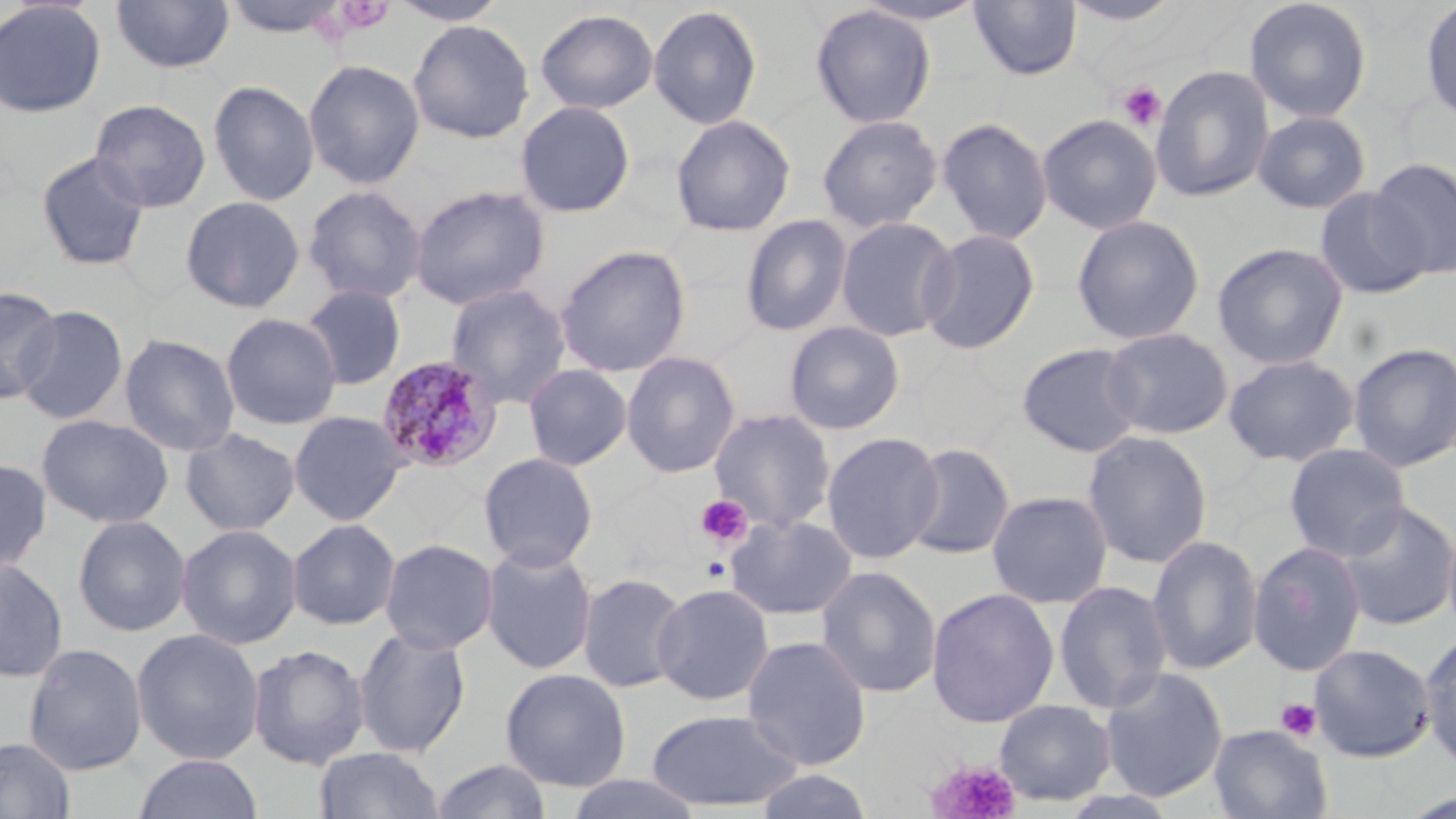

Summary:
  - Coordinate format: approximate bounding boxes as named x1/y1/x2/y2 corners in pixels
  - Uninfected red blood cell locations: (x1=111, y1=0, x2=234, y2=75), (x1=222, y1=0, x2=350, y2=38), (x1=388, y1=0, x2=509, y2=26), (x1=1243, y1=0, x2=1373, y2=123), (x1=0, y1=1, x2=107, y2=118), (x1=968, y1=1, x2=1082, y2=81), (x1=1060, y1=1, x2=1184, y2=28), (x1=1419, y1=1, x2=1456, y2=128), (x1=648, y1=4, x2=762, y2=129), (x1=810, y1=4, x2=936, y2=128), (x1=535, y1=8, x2=658, y2=114), (x1=408, y1=19, x2=534, y2=143), (x1=303, y1=59, x2=425, y2=189), (x1=1151, y1=64, x2=1275, y2=203), (x1=207, y1=79, x2=320, y2=206), (x1=89, y1=99, x2=211, y2=213), (x1=515, y1=101, x2=636, y2=218), (x1=1252, y1=110, x2=1371, y2=214), (x1=816, y1=114, x2=943, y2=232), (x1=1037, y1=114, x2=1163, y2=234), (x1=670, y1=115, x2=796, y2=237), (x1=937, y1=117, x2=1053, y2=245), (x1=36, y1=152, x2=150, y2=272), (x1=1369, y1=157, x2=1456, y2=280), (x1=302, y1=184, x2=428, y2=305), (x1=409, y1=185, x2=550, y2=310), (x1=1314, y1=187, x2=1432, y2=299), (x1=180, y1=195, x2=305, y2=313), (x1=740, y1=214, x2=853, y2=336), (x1=1071, y1=214, x2=1205, y2=345), (x1=836, y1=216, x2=958, y2=342), (x1=918, y1=228, x2=1040, y2=354), (x1=1211, y1=242, x2=1349, y2=370), (x1=555, y1=245, x2=691, y2=378), (x1=445, y1=282, x2=572, y2=409), (x1=300, y1=284, x2=407, y2=390), (x1=1, y1=286, x2=61, y2=404), (x1=14, y1=306, x2=128, y2=425), (x1=220, y1=313, x2=342, y2=430), (x1=783, y1=321, x2=905, y2=435), (x1=1101, y1=327, x2=1233, y2=440), (x1=119, y1=332, x2=240, y2=456), (x1=1347, y1=341, x2=1456, y2=472), (x1=1016, y1=342, x2=1145, y2=457), (x1=621, y1=351, x2=741, y2=477), (x1=1223, y1=354, x2=1359, y2=466), (x1=523, y1=363, x2=633, y2=472), (x1=709, y1=408, x2=837, y2=533), (x1=288, y1=410, x2=408, y2=526), (x1=36, y1=414, x2=174, y2=528), (x1=181, y1=427, x2=300, y2=536), (x1=1082, y1=430, x2=1213, y2=568), (x1=822, y1=431, x2=944, y2=564), (x1=903, y1=442, x2=1016, y2=562), (x1=1283, y1=443, x2=1411, y2=561), (x1=478, y1=452, x2=599, y2=573), (x1=0, y1=458, x2=52, y2=574), (x1=987, y1=489, x2=1113, y2=608), (x1=1334, y1=500, x2=1456, y2=631), (x1=726, y1=513, x2=858, y2=621), (x1=72, y1=514, x2=191, y2=637), (x1=287, y1=518, x2=401, y2=630), (x1=176, y1=524, x2=302, y2=650), (x1=1147, y1=534, x2=1263, y2=674), (x1=379, y1=538, x2=499, y2=655), (x1=1248, y1=541, x2=1366, y2=676), (x1=480, y1=545, x2=598, y2=675), (x1=0, y1=557, x2=68, y2=683), (x1=815, y1=565, x2=942, y2=699), (x1=577, y1=571, x2=689, y2=693), (x1=1053, y1=579, x2=1173, y2=714), (x1=652, y1=583, x2=775, y2=706), (x1=926, y1=587, x2=1059, y2=728), (x1=353, y1=624, x2=471, y2=758), (x1=131, y1=627, x2=265, y2=765), (x1=1419, y1=632, x2=1456, y2=768), (x1=742, y1=635, x2=872, y2=770), (x1=23, y1=643, x2=147, y2=776), (x1=1309, y1=643, x2=1435, y2=761), (x1=248, y1=644, x2=370, y2=770), (x1=1099, y1=666, x2=1228, y2=803), (x1=500, y1=668, x2=631, y2=791), (x1=994, y1=699, x2=1117, y2=806), (x1=645, y1=708, x2=803, y2=811), (x1=1208, y1=725, x2=1332, y2=818), (x1=0, y1=737, x2=76, y2=818), (x1=313, y1=745, x2=446, y2=818), (x1=133, y1=753, x2=264, y2=819), (x1=429, y1=759, x2=553, y2=818), (x1=754, y1=769, x2=875, y2=819), (x1=564, y1=774, x2=704, y2=819)
  - Platelet locations: (x1=333, y1=1, x2=394, y2=37), (x1=1117, y1=81, x2=1166, y2=131), (x1=696, y1=494, x2=753, y2=548), (x1=1275, y1=697, x2=1322, y2=742), (x1=927, y1=759, x2=1022, y2=819)
  - Plasmodium malariae-infected red blood cell locations: (x1=376, y1=356, x2=502, y2=474)
  - Slide-level diagnosis: Plasmodium malariae
  - Stain: May-Grünwald-Giemsa
  - Magnification: 1000x
  - Modality: light microscopy
  - Preparation: thin blood film
  - Image size: 1456×819 pixels
  - Field of view: single